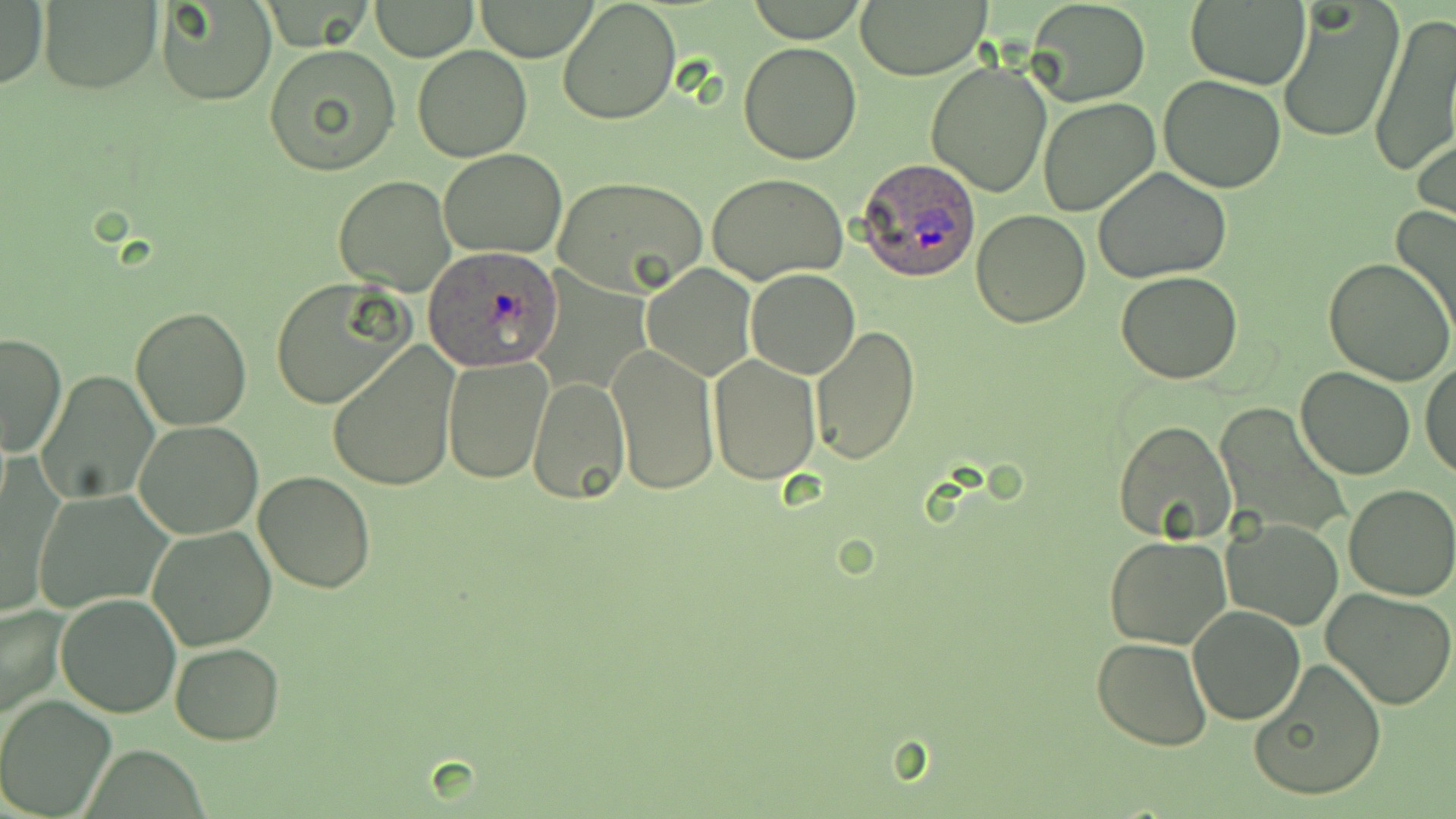
slide-level diagnosis = Plasmodium ovale
image size = 1456×819 pixels
modality = optical microscopy
field of view = single
Plasmodium ovale-infected red blood cell locations = approximate bounding boxes as (x1, y1, x2, y2) in pixels: (856, 157, 981, 281), (423, 247, 564, 370)
magnification = 1000x
preparation = thin blood film
uninfected red blood cell locations = approximate bounding boxes as (x1, y1, x2, y2) in pixels: (154, 0, 275, 105), (557, 0, 682, 125), (1025, 0, 1151, 108), (1185, 0, 1311, 91), (0, 1, 48, 92), (368, 1, 478, 62), (472, 1, 601, 61), (745, 1, 870, 43), (856, 1, 988, 79), (39, 2, 156, 92), (1279, 4, 1400, 144), (1366, 16, 1454, 181), (738, 41, 863, 165), (265, 44, 401, 175), (412, 44, 533, 162), (926, 61, 1053, 196), (1158, 75, 1287, 192), (1037, 97, 1160, 217), (1414, 126, 1456, 237), (440, 147, 568, 259), (1092, 166, 1234, 283), (706, 173, 850, 285), (335, 176, 456, 295), (553, 176, 709, 299), (1389, 204, 1456, 339), (971, 210, 1092, 329), (1323, 259, 1455, 387), (642, 264, 756, 381), (747, 268, 860, 378), (1117, 270, 1241, 384), (268, 280, 409, 411), (130, 305, 252, 430), (809, 326, 922, 466), (1, 333, 67, 456), (610, 343, 718, 495), (328, 344, 460, 493), (709, 353, 819, 483), (442, 356, 552, 484), (1420, 362, 1455, 482), (1295, 366, 1416, 479), (36, 370, 159, 505), (525, 373, 630, 505), (1218, 403, 1349, 539), (133, 419, 264, 539), (1112, 419, 1238, 545), (252, 470, 378, 594), (1342, 484, 1456, 599), (36, 489, 170, 612), (1222, 518, 1344, 631), (146, 525, 275, 648), (1105, 536, 1231, 649), (1323, 589, 1456, 712), (56, 593, 180, 718), (0, 602, 67, 721), (1188, 605, 1307, 727), (1092, 636, 1214, 750), (170, 642, 283, 745), (1248, 658, 1388, 803), (0, 693, 117, 819)
stain = May-Grünwald-Giemsa